Assess the morphology of the erythrocytes.
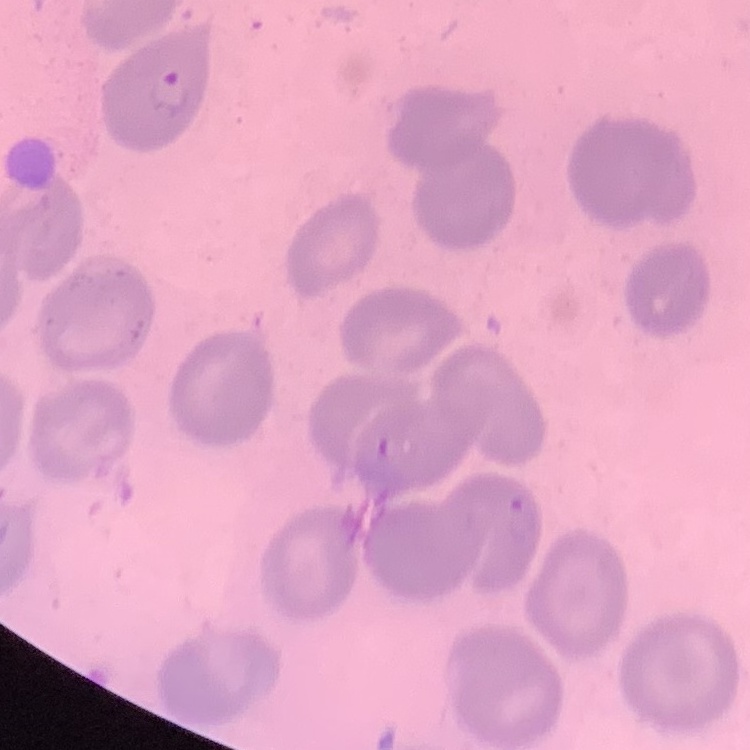

They show no rouleaux formation.

Field's or Giemsa stain. Thin peripheral smear. Square crop of a larger photomicrograph.